Assess this cell for malaria.
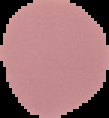

It is uninfected.

preparation = thin blood smear
image size = 109×118 pixels
image type = segmented cell region on a black background